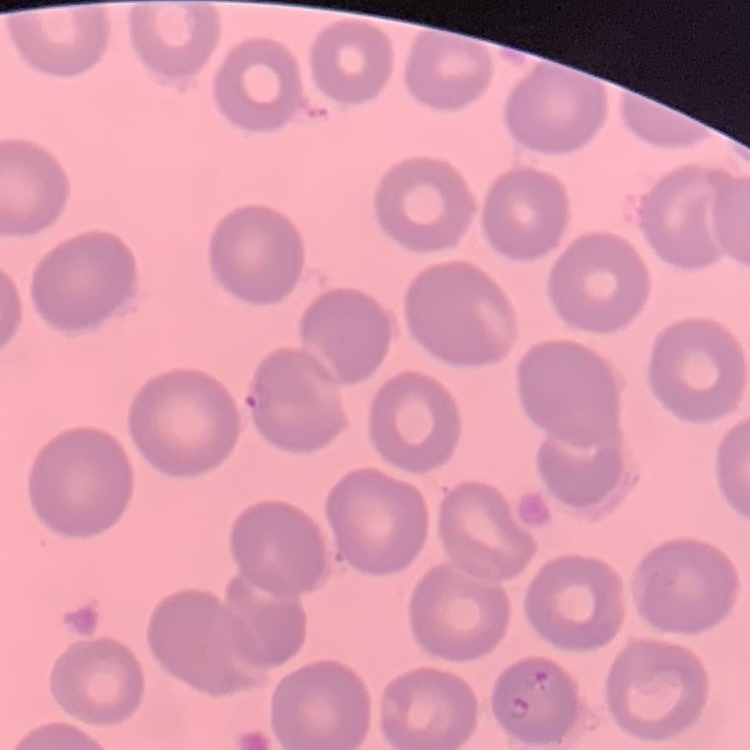 The erythrocytes exhibit no rouleaux formation. Thin blood film. Field's or Giemsa stain. One tile cut from a larger photomicrograph.